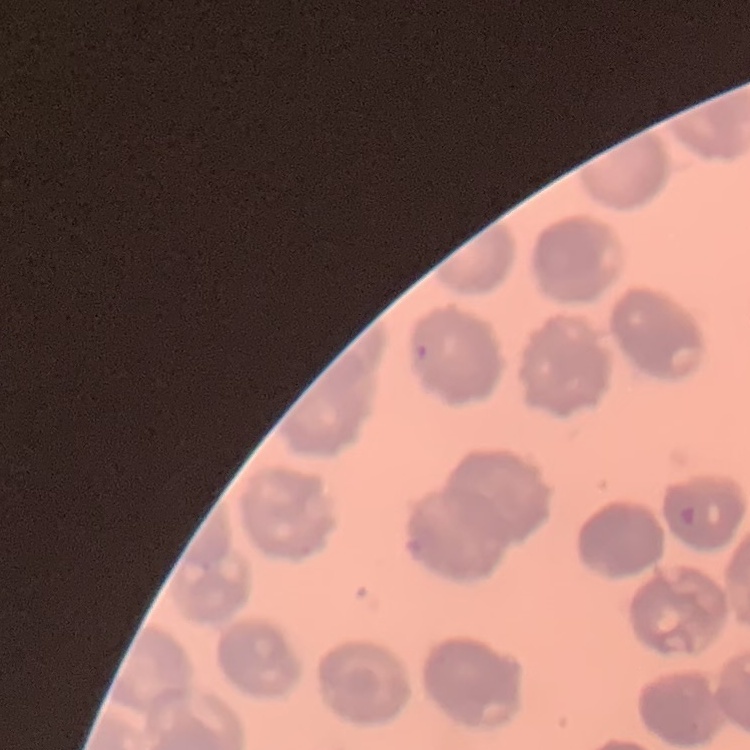

erythrocyte morphology = no rouleaux formation
preparation = thin blood smear
stain = Field's or Giemsa
image type = square crop of a larger photomicrograph